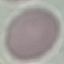

Malaria status: uninfected. Acquired by smartphone through the microscope eyepiece. Automatically extracted cell patch, resized to 64 × 64 pixels. Giemsa-stained preparation. Thin blood smear.